Comment on the morphology of the red blood cells.
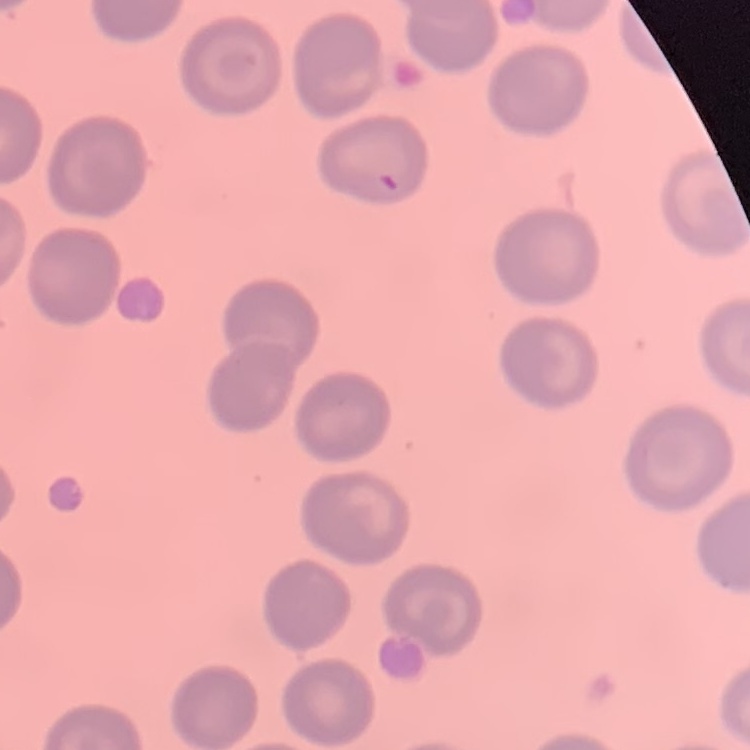
No rouleaux formation.

Thin blood smear. One tile cut from a larger photomicrograph. Field's or Giemsa stain.